Identify the parasite.
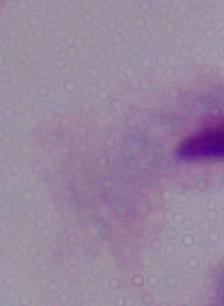

A trichomonad.

Captured at 1000x magnification. Micrograph.